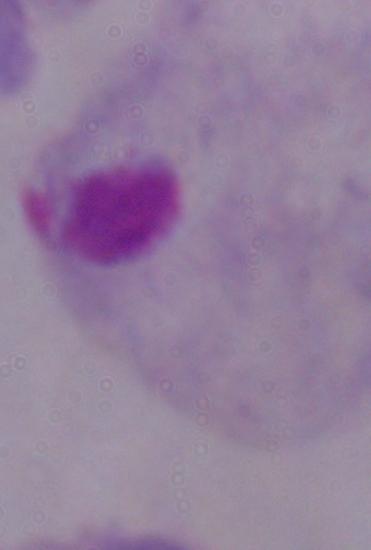
magnification = 1000x
modality = photomicrograph
identification = trichomonad